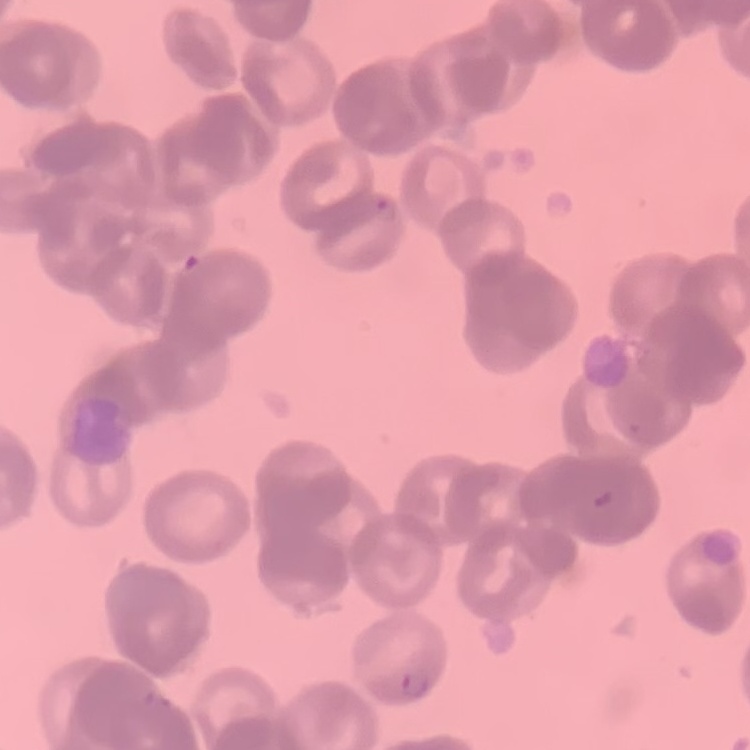
Summary:
  - Erythrocyte morphology: rouleaux formation
  - Preparation: thin blood smear
  - Image type: square crop of a larger photomicrograph
  - Stain: Field's or Giemsa